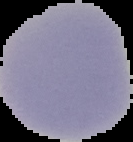

From a thin blood film. Image is 133×142 pixels. Malaria status: uninfected. Cell region segmented out of the field of view; the surrounding area is masked to black.